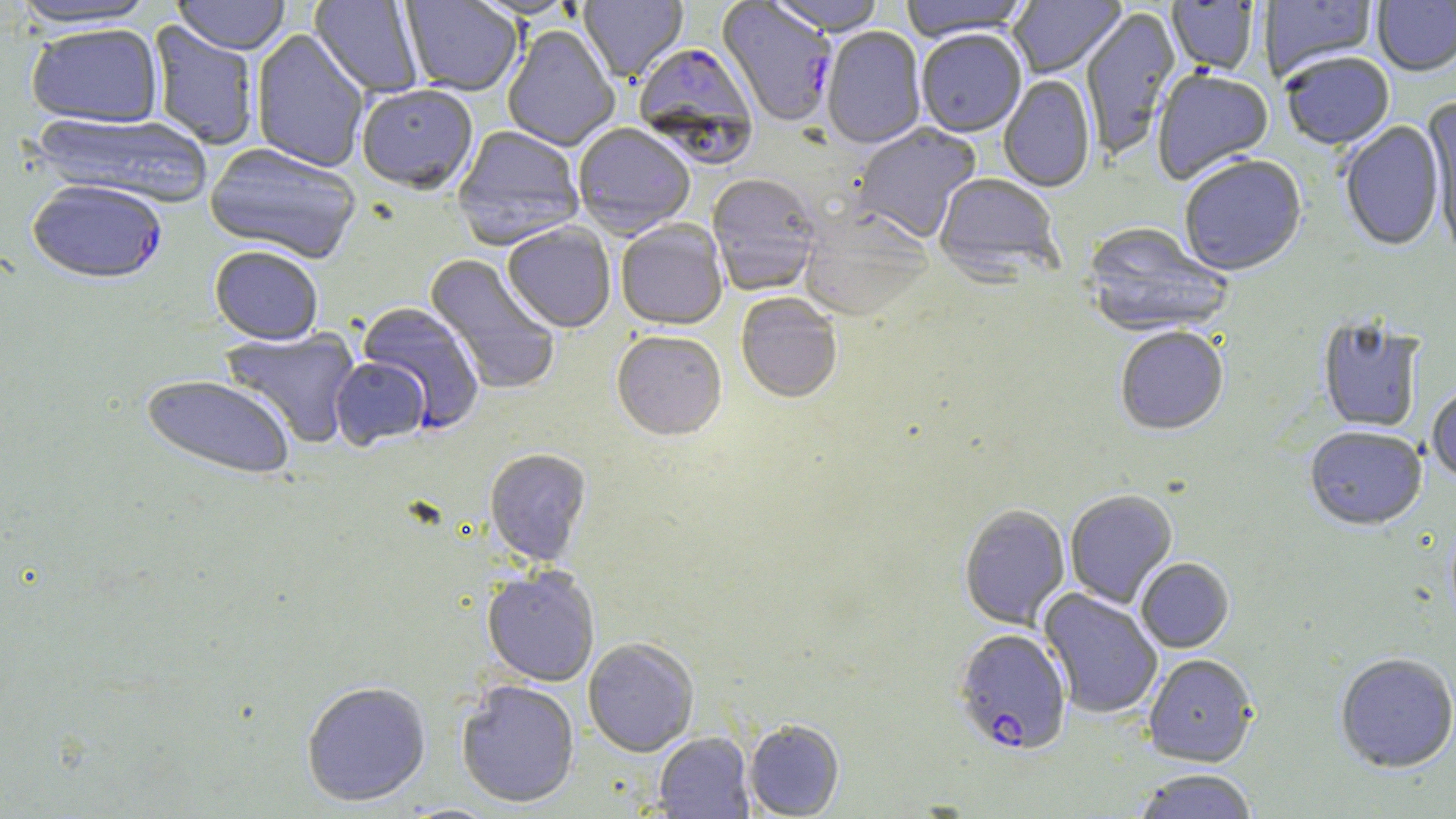 Approximate bounding boxes as [x1, y1, x2, y2] in pixels. Plasmodium falciparum-infected red blood cell locations: [717, 2, 837, 129], [633, 43, 756, 163], [27, 181, 168, 286], [356, 302, 485, 434], [953, 629, 1072, 756]. Uninfected red blood cell locations: [6, 0, 160, 31], [173, 0, 290, 55], [309, 0, 424, 98], [579, 0, 688, 84], [765, 0, 887, 39], [899, 0, 1033, 43], [1008, 0, 1126, 79], [1260, 0, 1377, 82], [401, 1, 522, 97], [1167, 1, 1259, 76], [1372, 1, 1456, 78], [1007, 3, 1114, 162], [1081, 7, 1180, 161], [147, 20, 259, 151], [26, 24, 163, 127], [502, 26, 619, 152], [822, 28, 926, 151], [251, 29, 369, 173], [916, 32, 1027, 139], [1282, 55, 1394, 152], [1152, 70, 1273, 185], [998, 76, 1095, 194], [357, 87, 478, 196], [1421, 99, 1456, 254], [30, 111, 213, 209], [1339, 121, 1446, 253], [851, 124, 982, 244], [573, 125, 695, 240], [451, 127, 584, 251], [205, 143, 361, 265], [1179, 158, 1307, 278], [707, 175, 822, 297], [933, 175, 1062, 284], [799, 211, 933, 323], [615, 221, 728, 332], [502, 223, 616, 334], [1082, 223, 1234, 339], [209, 247, 324, 347], [424, 253, 561, 396], [735, 294, 842, 405], [1317, 318, 1425, 434], [219, 327, 361, 449], [1115, 328, 1229, 437], [611, 333, 727, 444], [330, 358, 432, 452], [140, 375, 294, 483], [1427, 385, 1456, 486], [1304, 428, 1427, 532], [484, 450, 592, 568], [1065, 491, 1178, 609], [959, 505, 1070, 631], [1136, 559, 1234, 653], [482, 569, 600, 688], [1038, 589, 1162, 719], [583, 639, 699, 758], [1143, 654, 1258, 767], [1334, 654, 1455, 775], [456, 681, 580, 809], [301, 682, 431, 808], [743, 721, 845, 818], [653, 733, 754, 818], [1133, 770, 1258, 819]. Slide-level diagnosis: Plasmodium falciparum. Light microscopy. 1000x magnification. Image is 1456×819 pixels. Thin blood film. Single field of view. May-Grünwald-Giemsa stain.